Locate every Plasmodium vivax-infected red blood cell.
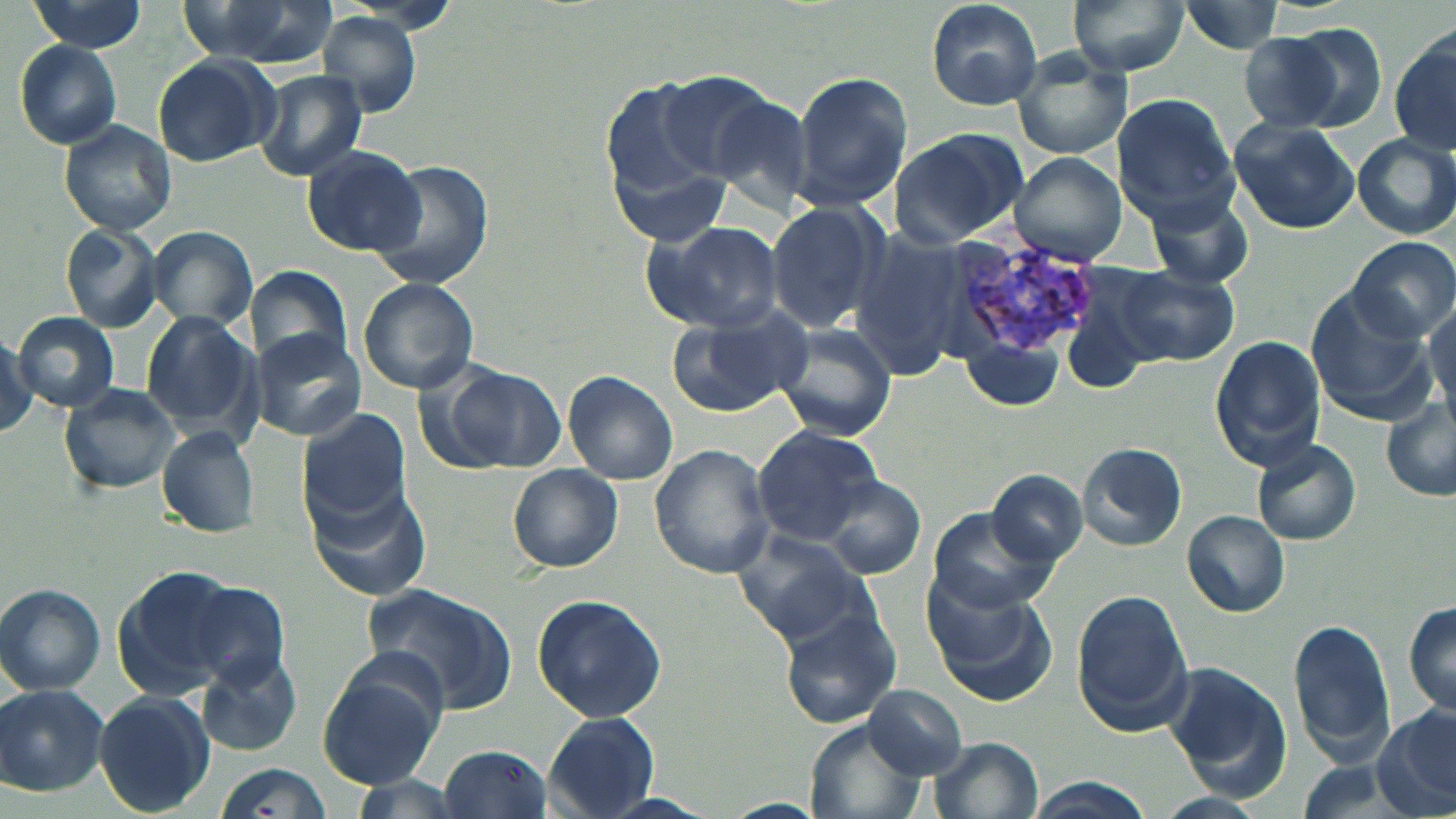

Approximate bounding boxes as named x1/y1/x2/y2 corners in pixels.
Plasmodium vivax-infected red blood cells: (x1=943, y1=237, x2=1098, y2=358).

Summary:
  - Uninfected red blood cell locations: (x1=176, y1=0, x2=338, y2=67), (x1=923, y1=0, x2=1043, y2=112), (x1=1062, y1=0, x2=1190, y2=76), (x1=1176, y1=0, x2=1291, y2=56), (x1=27, y1=2, x2=149, y2=52), (x1=319, y1=13, x2=423, y2=116), (x1=1284, y1=24, x2=1389, y2=131), (x1=1390, y1=29, x2=1456, y2=157), (x1=1239, y1=34, x2=1350, y2=131), (x1=13, y1=40, x2=123, y2=148), (x1=1012, y1=49, x2=1133, y2=161), (x1=152, y1=53, x2=280, y2=165), (x1=258, y1=71, x2=367, y2=182), (x1=791, y1=72, x2=911, y2=212), (x1=654, y1=73, x2=785, y2=181), (x1=599, y1=86, x2=733, y2=242), (x1=1110, y1=92, x2=1238, y2=218), (x1=1229, y1=117, x2=1359, y2=234), (x1=61, y1=120, x2=178, y2=236), (x1=888, y1=127, x2=1028, y2=248), (x1=1352, y1=134, x2=1456, y2=238), (x1=300, y1=145, x2=427, y2=257), (x1=1011, y1=153, x2=1128, y2=266), (x1=364, y1=159, x2=495, y2=292), (x1=1146, y1=190, x2=1256, y2=290), (x1=765, y1=202, x2=889, y2=333), (x1=643, y1=220, x2=785, y2=334), (x1=61, y1=224, x2=165, y2=332), (x1=146, y1=224, x2=259, y2=333), (x1=1347, y1=236, x2=1455, y2=341), (x1=1111, y1=263, x2=1239, y2=366), (x1=1058, y1=265, x2=1166, y2=392), (x1=244, y1=266, x2=352, y2=370), (x1=357, y1=277, x2=478, y2=394), (x1=1306, y1=288, x2=1437, y2=423), (x1=1424, y1=301, x2=1456, y2=424), (x1=667, y1=304, x2=810, y2=416), (x1=12, y1=311, x2=118, y2=413), (x1=140, y1=312, x2=261, y2=439), (x1=773, y1=323, x2=897, y2=440), (x1=247, y1=329, x2=365, y2=440), (x1=0, y1=333, x2=40, y2=437), (x1=1210, y1=335, x2=1325, y2=467), (x1=958, y1=341, x2=1068, y2=411), (x1=436, y1=365, x2=566, y2=474), (x1=564, y1=371, x2=679, y2=485), (x1=58, y1=382, x2=182, y2=496), (x1=1381, y1=400, x2=1456, y2=502), (x1=298, y1=407, x2=411, y2=523), (x1=751, y1=424, x2=882, y2=543), (x1=157, y1=426, x2=260, y2=538), (x1=1251, y1=438, x2=1361, y2=545), (x1=1076, y1=441, x2=1187, y2=551), (x1=649, y1=444, x2=774, y2=579), (x1=509, y1=465, x2=623, y2=572), (x1=986, y1=472, x2=1087, y2=565), (x1=817, y1=475, x2=927, y2=579), (x1=307, y1=481, x2=435, y2=601), (x1=924, y1=508, x2=1057, y2=616), (x1=1181, y1=508, x2=1291, y2=618), (x1=731, y1=529, x2=879, y2=643), (x1=115, y1=566, x2=269, y2=690), (x1=924, y1=577, x2=1054, y2=705), (x1=175, y1=581, x2=296, y2=744), (x1=359, y1=583, x2=518, y2=716), (x1=1, y1=584, x2=105, y2=696), (x1=1072, y1=591, x2=1194, y2=730), (x1=531, y1=593, x2=667, y2=721), (x1=1403, y1=601, x2=1456, y2=718), (x1=781, y1=610, x2=903, y2=728), (x1=1289, y1=620, x2=1395, y2=763), (x1=199, y1=655, x2=303, y2=757), (x1=318, y1=656, x2=446, y2=787), (x1=1163, y1=664, x2=1288, y2=788), (x1=1, y1=685, x2=109, y2=796), (x1=863, y1=685, x2=967, y2=778), (x1=92, y1=691, x2=216, y2=816), (x1=1375, y1=704, x2=1456, y2=816), (x1=543, y1=713, x2=660, y2=817), (x1=806, y1=720, x2=925, y2=819), (x1=925, y1=736, x2=1044, y2=819), (x1=439, y1=744, x2=554, y2=817), (x1=206, y1=765, x2=335, y2=818), (x1=1017, y1=779, x2=1158, y2=819)
  - Slide-level diagnosis: Plasmodium vivax
  - Modality: optical microscopy
  - Preparation: thin blood smear
  - Field of view: single
  - Magnification: 1000x
  - Stain: May-Grünwald-Giemsa
  - Image size: 1456×819 pixels